Locate every blood parasite and identify its species.
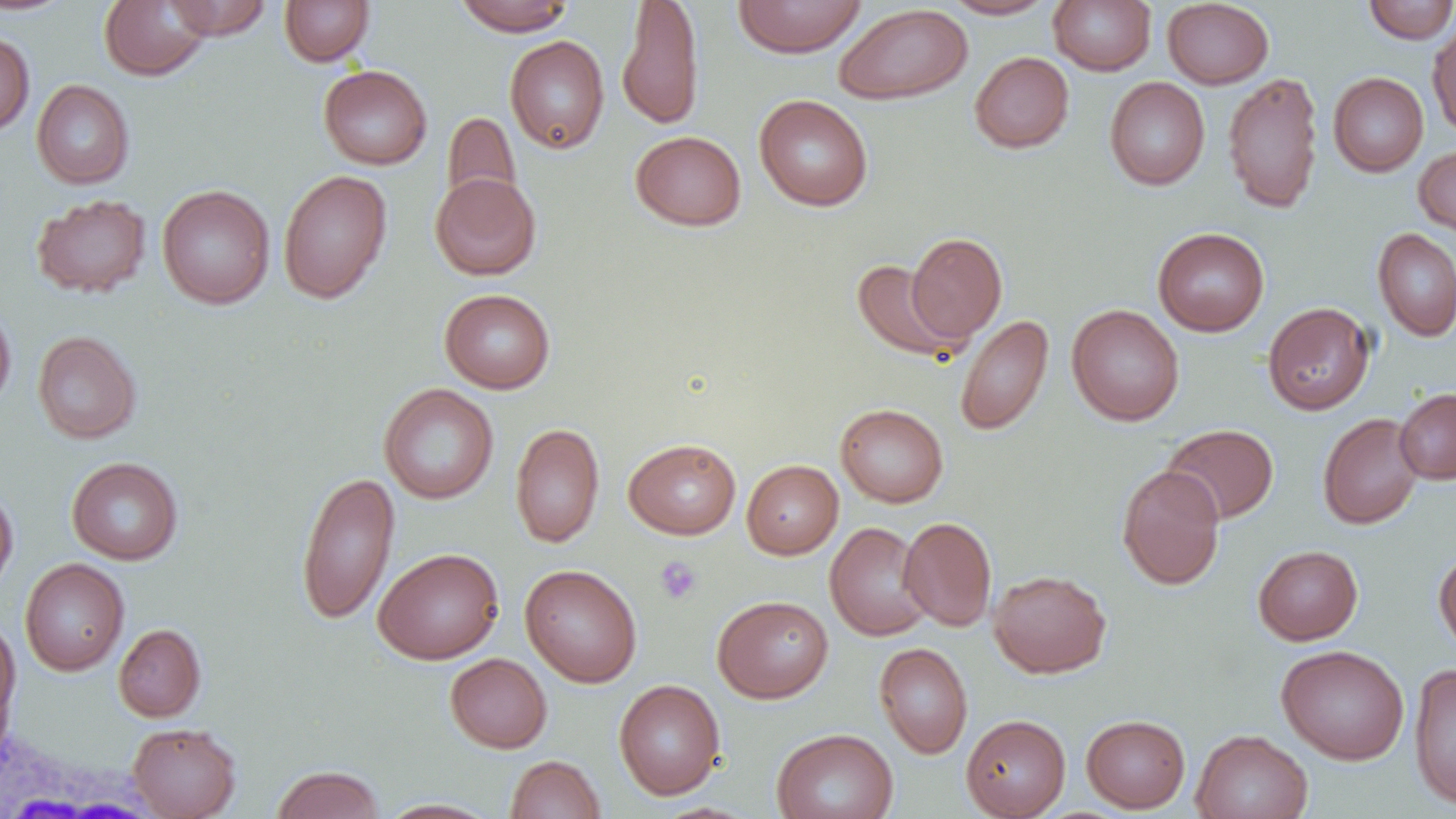

No blood parasites seen.

slide_level_diagnosis: negative for blood parasites
uninfected_red_blood_cell_locations: 'approximate bounding boxes as [x1, y1, x2, y2] in pixels: [0, 0, 76, 15], [163, 0, 273, 40], [279, 0, 375, 67], [453, 0, 576, 35], [616, 0, 704, 130], [732, 0, 867, 58], [941, 0, 1057, 19], [1048, 0, 1156, 75], [1162, 0, 1274, 89], [99, 1, 212, 81], [1362, 1, 1456, 44], [834, 3, 973, 105], [1427, 21, 1456, 140], [0, 31, 35, 137], [504, 35, 610, 154], [969, 51, 1074, 153], [318, 65, 432, 170], [1222, 71, 1324, 214], [1328, 72, 1429, 177], [1104, 77, 1210, 190], [31, 80, 135, 189], [754, 94, 873, 211], [442, 111, 521, 211], [630, 130, 746, 230], [1414, 145, 1456, 238], [278, 169, 393, 304], [430, 172, 541, 280], [157, 184, 275, 310], [30, 193, 152, 298], [1153, 227, 1269, 336], [1373, 228, 1456, 342], [906, 232, 1008, 343], [852, 258, 964, 363], [439, 288, 555, 394], [1262, 301, 1375, 415], [0, 302, 16, 412], [1067, 304, 1184, 426], [955, 315, 1054, 436], [32, 331, 142, 444], [379, 383, 499, 505], [1395, 388, 1456, 484], [835, 403, 949, 507], [1317, 412, 1424, 529], [510, 423, 605, 547], [1161, 423, 1279, 525], [623, 438, 741, 539], [66, 456, 183, 565], [742, 460, 843, 559], [1116, 464, 1226, 590], [296, 470, 400, 626], [0, 487, 18, 596], [899, 516, 997, 631], [824, 522, 933, 641], [1253, 545, 1363, 645], [373, 546, 504, 665], [1434, 547, 1456, 658], [19, 558, 129, 676], [520, 564, 643, 687], [989, 569, 1112, 678], [712, 594, 833, 703], [0, 619, 20, 739], [113, 623, 207, 722], [874, 642, 973, 758], [1276, 644, 1410, 764], [445, 653, 552, 753], [1409, 663, 1456, 810], [613, 679, 726, 800], [960, 714, 1071, 819], [1081, 714, 1191, 812], [128, 722, 242, 818], [770, 727, 899, 819], [1191, 729, 1313, 819], [505, 754, 605, 818], [271, 765, 384, 818], [378, 798, 502, 818]'
white_blood_cell_locations: 'approximate bounding boxes as [x1, y1, x2, y2] in pixels: [0, 721, 157, 819]'
field_of_view: single
modality: optical microscopy
magnification: 1000x
image_size: 1456×819 pixels
platelet_locations: 'approximate bounding boxes as [x1, y1, x2, y2] in pixels: [654, 555, 702, 605]'
preparation: thin blood film